Locate and identify every blood parasite.
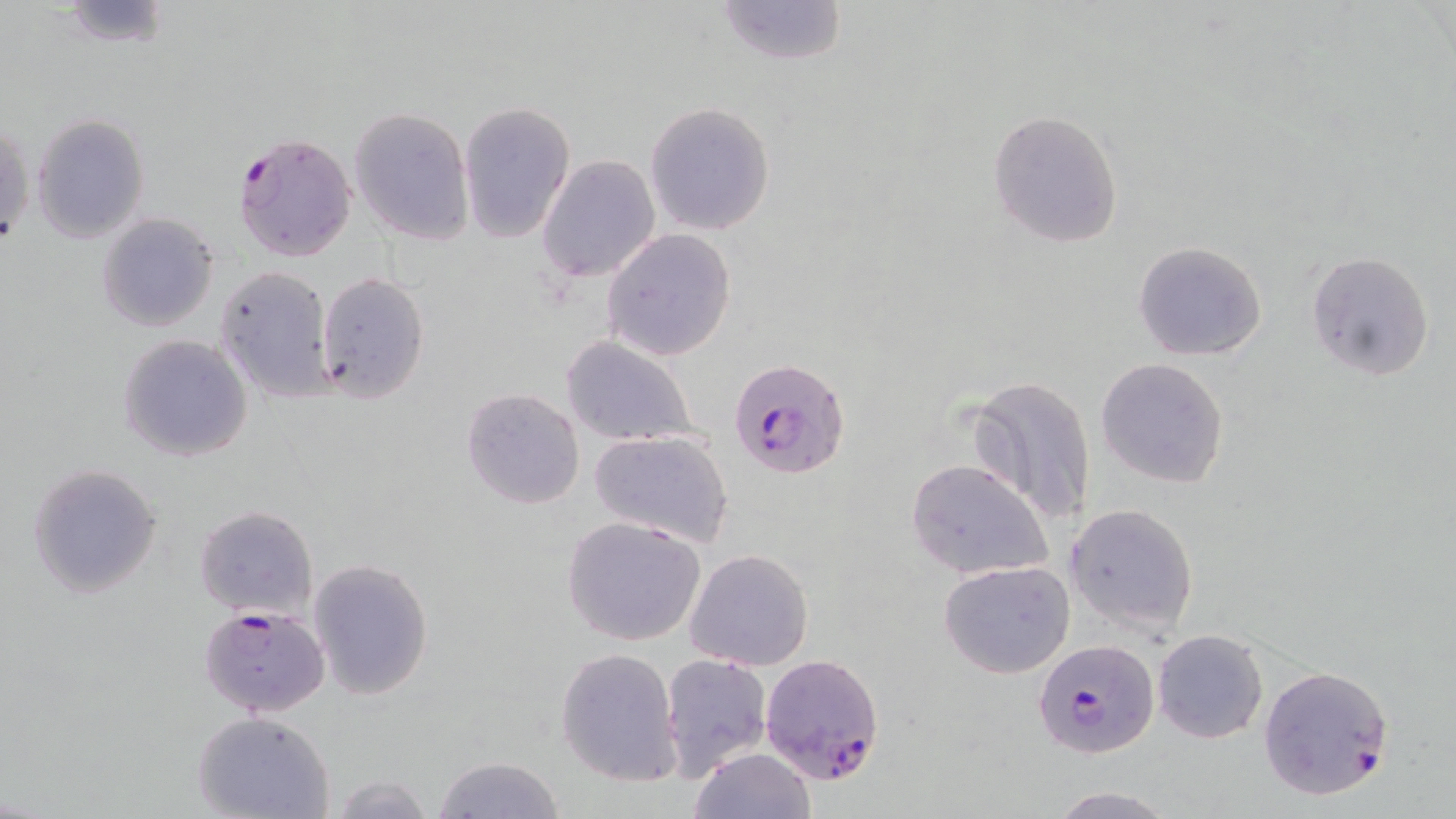
Approximate bounding boxes as [x1, y1, x2, y2] in pixels.
Plasmodium falciparum-infected red blood cells: [230, 131, 358, 264], [728, 358, 850, 479], [198, 605, 331, 717], [1028, 642, 1156, 759], [759, 653, 886, 786], [1256, 665, 1394, 800].
No Plasmodium ovale, Plasmodium malariae, Plasmodium vivax, Babesia divergens, or Trypanosoma brucei observed.

Uninfected red blood cell locations: [54, 0, 175, 50], [714, 0, 848, 67], [645, 100, 775, 236], [458, 101, 575, 243], [348, 106, 474, 245], [987, 108, 1123, 250], [30, 113, 149, 244], [1, 118, 33, 250], [537, 153, 659, 283], [97, 213, 218, 332], [601, 229, 736, 361], [1132, 239, 1268, 362], [1304, 249, 1435, 381], [215, 266, 335, 402], [315, 270, 430, 404], [118, 334, 253, 462], [559, 335, 701, 446], [1096, 357, 1229, 488], [966, 375, 1097, 527], [461, 387, 585, 509], [589, 428, 735, 548], [905, 458, 1055, 581], [28, 463, 163, 600], [1065, 502, 1200, 637], [195, 504, 319, 620], [563, 515, 707, 647], [684, 548, 815, 671], [308, 558, 436, 700], [938, 561, 1076, 679], [1152, 629, 1268, 744], [556, 647, 684, 787], [660, 653, 773, 781], [192, 710, 334, 819], [686, 748, 816, 819], [431, 756, 569, 818], [328, 773, 437, 818], [1045, 787, 1181, 818]. Slide-level diagnosis: Plasmodium falciparum. One field of a larger specimen. Optical microscopy. Thin blood smear. May-Grünwald-Giemsa stain. Image is 1456×819 pixels. Captured at 1000x magnification.